Assess this cell for malaria.
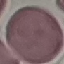

Uninfected.

Summary:
  - Stain: Giemsa
  - Preparation: thin blood smear
  - Capture: smartphone through the microscope eyepiece
  - Image type: automatically extracted cell patch, resized to 64 × 64 pixels